Find the red blood cells that are infected with P. falciparum, and any of indeterminate infection status.
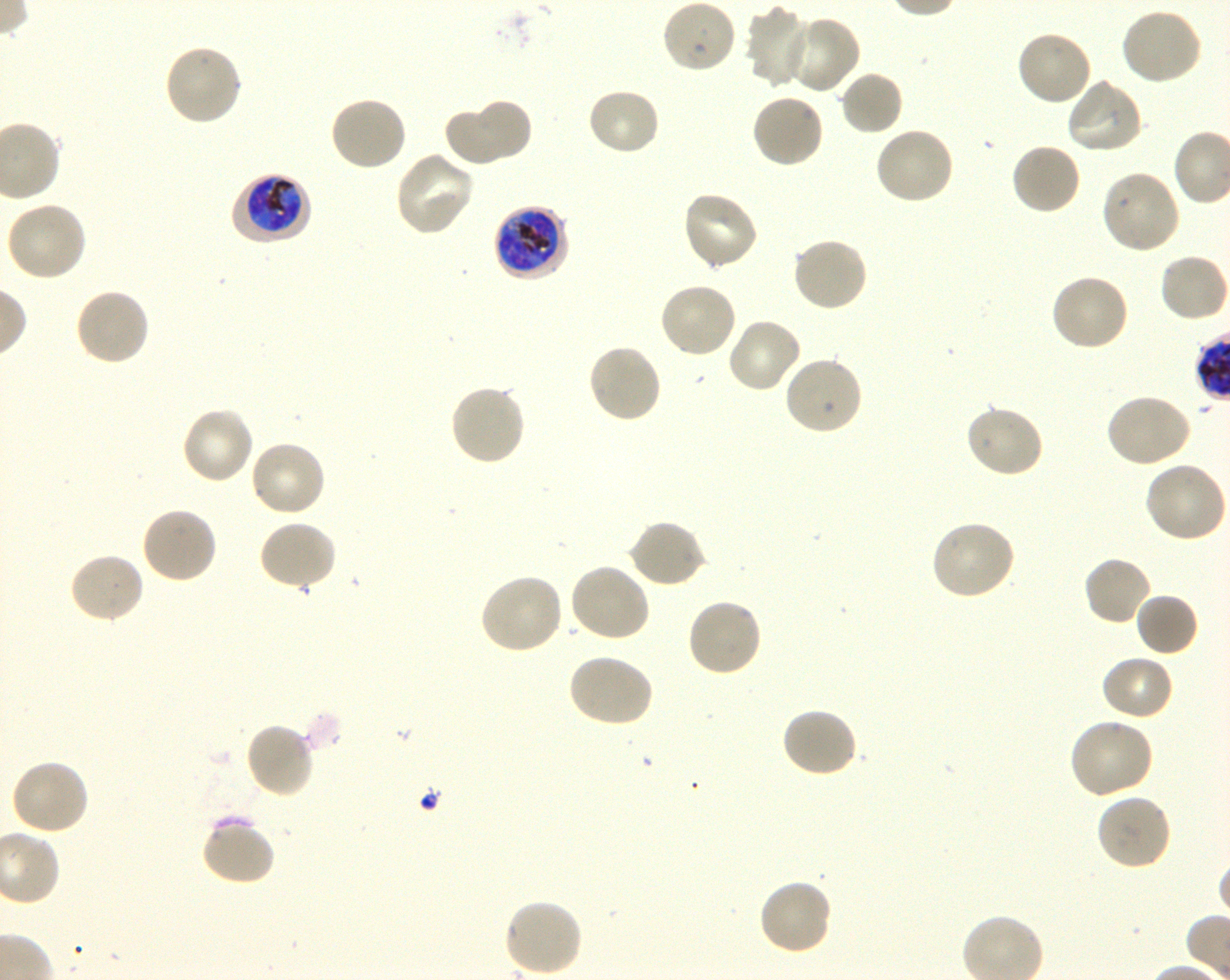
Approximate bounding boxes as {x1, y1, x2, y2} in pixels. Not every red blood cell is marked. A life-cycle stage — or a range of stages, where the recorded stages span more than one — follows each staged infected red blood cell.
Infected red blood cells: {232, 171, 312, 245} early trophozoite to early schizont; {493, 204, 571, 282} late trophozoite to late schizont.
No red blood cells of indeterminate infection status observed.

Summary:
  - Locations of uninfected red blood cells: {661, 0, 737, 74}, {746, 6, 814, 88}, {1120, 7, 1205, 86}, {784, 14, 862, 95}, {1015, 28, 1093, 107}, {163, 42, 244, 127}, {838, 70, 904, 137}, {1065, 77, 1144, 156}, {586, 87, 661, 157}, {750, 93, 826, 169}, {328, 95, 408, 173}, {472, 97, 532, 161}, {443, 105, 513, 167}, {874, 125, 956, 206}, {1010, 142, 1082, 217}, {393, 150, 476, 237}, {1100, 168, 1182, 255}, {680, 190, 760, 271}, {5, 199, 88, 282}, {791, 236, 868, 314}, {1158, 252, 1229, 323}, {1049, 273, 1131, 353}, {659, 280, 739, 358}, {74, 287, 152, 367}, {725, 317, 803, 395}, {586, 342, 663, 425}, {783, 355, 864, 436}, {447, 384, 527, 467}, {1105, 393, 1193, 469}, {964, 403, 1044, 479}, {180, 406, 256, 485}, {249, 439, 328, 518}, {1140, 462, 1227, 544}, {140, 505, 219, 584}, {930, 518, 1016, 601}, {628, 519, 708, 589}, {257, 520, 338, 592}, {68, 552, 145, 625}, {1082, 555, 1154, 627}, {568, 562, 653, 643}, {479, 571, 565, 655}, {1134, 591, 1200, 657}, {685, 597, 763, 677}, {566, 653, 655, 728}, {1100, 654, 1175, 722}, {781, 706, 859, 778}, {1067, 717, 1154, 800}, {244, 721, 316, 799}, {10, 758, 90, 837}, {1095, 791, 1172, 871}, {200, 816, 276, 886}, {757, 877, 834, 956}, {504, 898, 583, 977}
  - Objective: 100x, oil immersion, numerical aperture 1.30
  - Image size: 1230×980 pixels
  - Preparation: thin blood smear
  - Field of view: single
  - Culture: P. falciparum strain 3D7, shaking, in vitro
  - Stain: Giemsa
  - Donor blood group: O+